Classify this cell by malaria status.
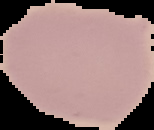

It is uninfected.

{
  "preparation": "thin blood smear",
  "image_type": "cell region segmented out of the field of view; surrounding area masked to black",
  "image_size": "154×130 pixels"
}